Evaluate for Plasmodium parasites.
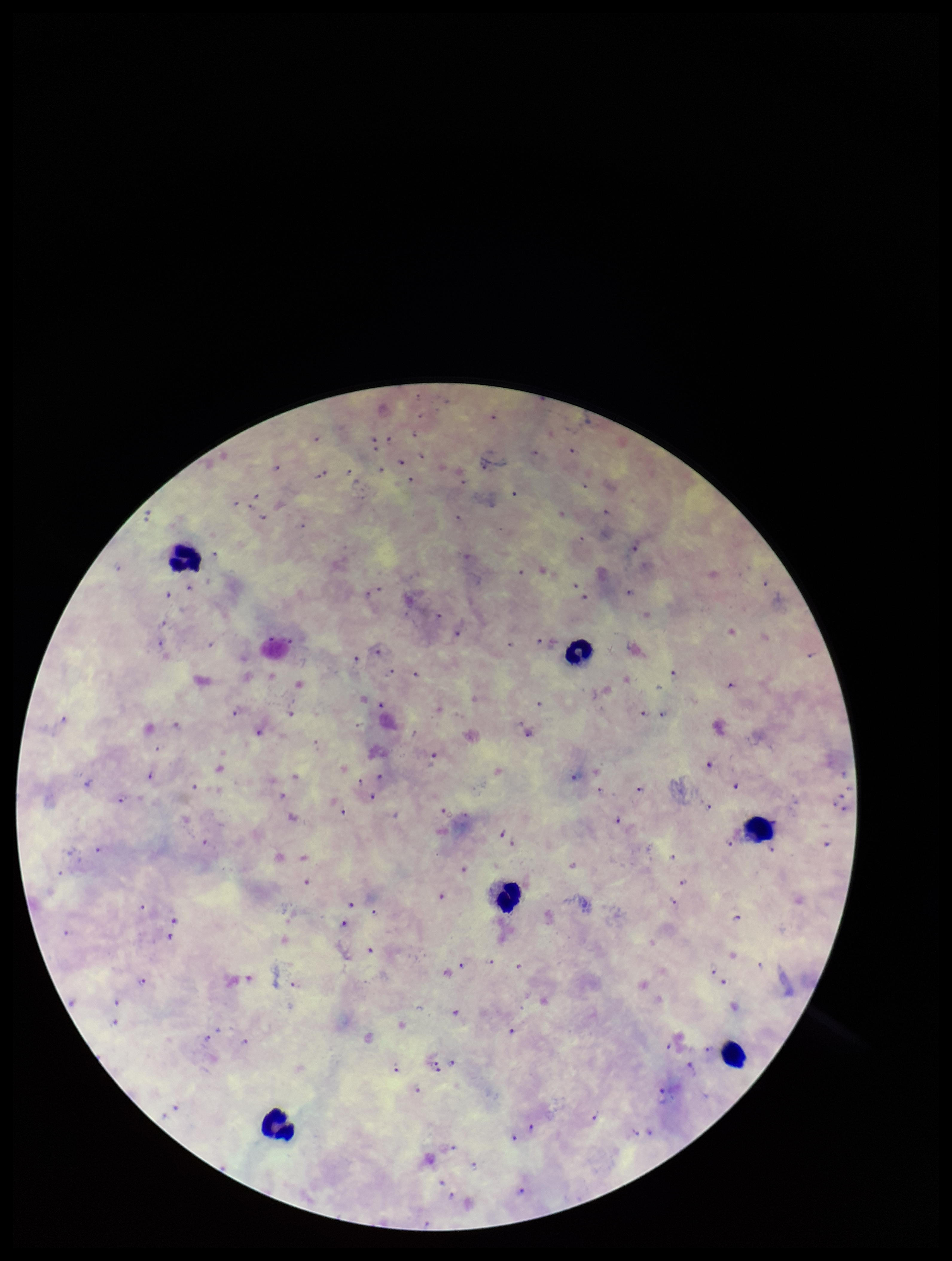

Identified.

Summary:
  - Species reported for this patient: Plasmodium falciparum
  - Capture: smartphone photograph through the microscope eyepiece
  - Parasite count: 115
  - Stain: Giemsa
  - Image size: 952×1261 pixels
  - Field of view: one from this slide
  - Preparation: thick smear
  - Leukocyte count: 6
  - Patient malaria status: positive